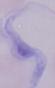 1000x magnification. A trypanosome is shown. Photomicrograph.